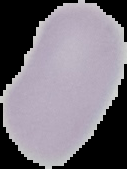

preparation: thin blood film
result: no Plasmodium parasites seen
image_type: segmented cell region on a black background
image_size: 127×169 pixels